State the preparation type.
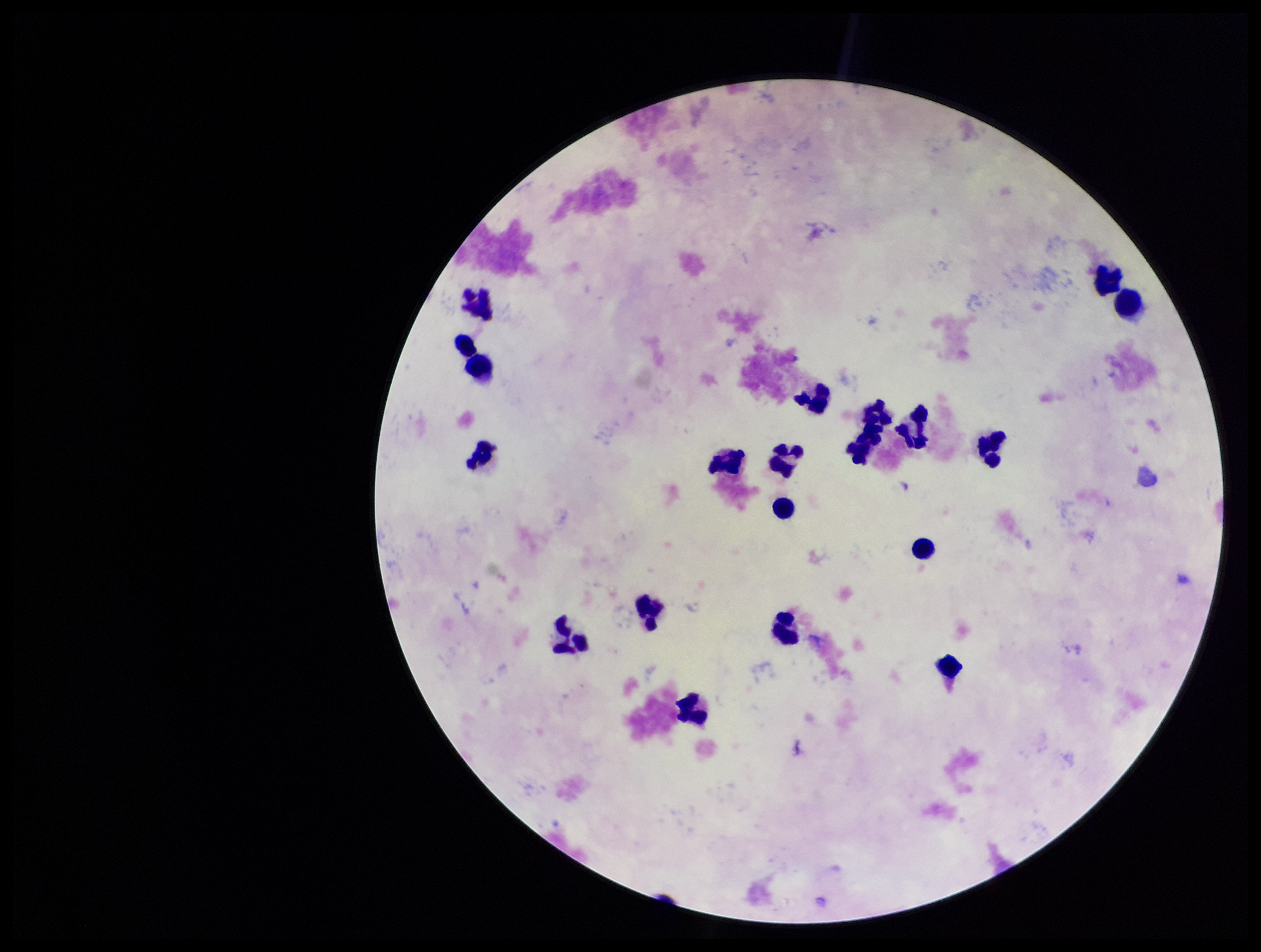

Thick.

Summary:
  - Stain: Giemsa
  - Parasite count: 0
  - Image size: 1261×952 pixels
  - Plasmodium parasites: none seen
  - Capture: smartphone photograph through the microscope eyepiece
  - Field of view: one from this slide
  - Leukocyte count: 20
  - Patient malaria status: negative